Identify the parasite.
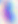
This is Toxoplasma gondii.

400x magnification. Micrograph.